Give a bounding box for every malaria parasite.
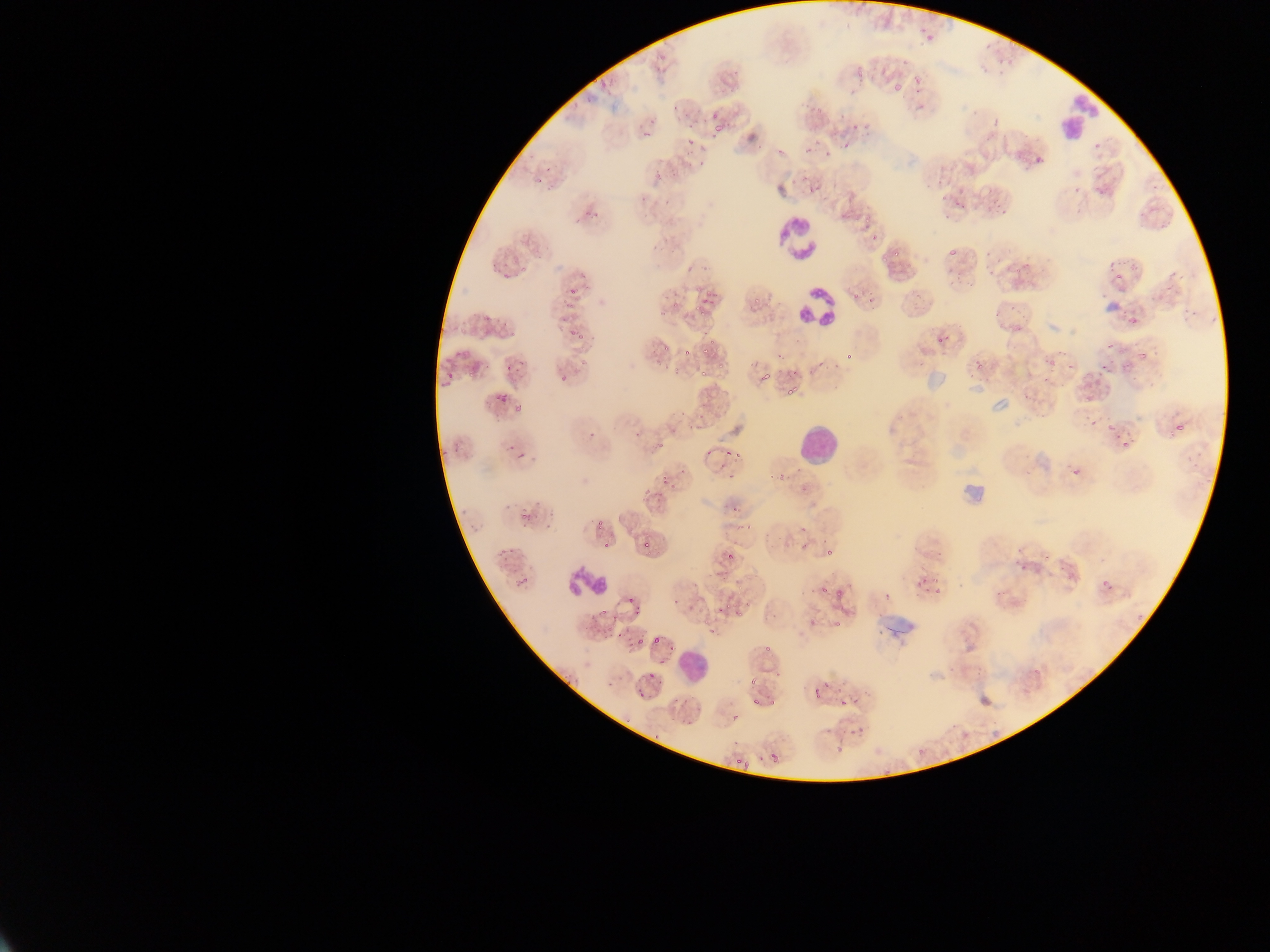
Approximate bounding boxes as (left, top, right, bottom) in pixels.
Malaria parasites (some below the resolvable threshold): (918, 27, 928, 38), (924, 32, 937, 42), (982, 38, 992, 51), (1004, 51, 1010, 71), (993, 52, 1004, 65), (652, 62, 664, 77), (856, 64, 865, 84), (893, 72, 908, 90), (596, 73, 614, 87), (912, 75, 920, 86), (804, 98, 825, 115), (710, 110, 721, 120), (838, 112, 846, 120), (685, 115, 701, 128), (713, 119, 730, 133), (641, 123, 656, 141), (865, 123, 879, 135), (853, 125, 862, 131), (842, 135, 859, 158), (684, 138, 696, 146), (801, 138, 818, 157), (696, 145, 706, 156), (775, 145, 784, 158), (822, 146, 833, 161), (1032, 149, 1045, 166), (696, 161, 705, 168), (652, 170, 660, 179), (803, 175, 817, 194), (1092, 182, 1105, 196), (663, 190, 673, 204), (952, 192, 966, 208), (1001, 197, 1014, 210), (990, 204, 1000, 217), (857, 212, 872, 230), (1159, 219, 1169, 229), (869, 233, 882, 243), (894, 248, 902, 258), (946, 248, 960, 257), (877, 254, 888, 266), (1012, 258, 1029, 275), (1104, 259, 1113, 270), (1125, 260, 1139, 269), (987, 263, 997, 275), (518, 267, 526, 275), (948, 271, 961, 288), (1170, 271, 1183, 280), (966, 281, 974, 288), (1162, 281, 1174, 294), (564, 283, 578, 295), (692, 284, 705, 295), (703, 284, 714, 305), (867, 288, 878, 307), (852, 291, 860, 303), (915, 292, 921, 301), (752, 295, 761, 307), (565, 301, 576, 314), (670, 301, 678, 309), (1008, 304, 1015, 313), (1180, 306, 1192, 321), (695, 308, 706, 318), (1126, 309, 1141, 326), (1207, 311, 1218, 323), (483, 313, 491, 320), (556, 318, 566, 322), (501, 319, 508, 330), (567, 327, 578, 338), (577, 330, 586, 344), (699, 330, 712, 338), (937, 333, 948, 344), (1104, 340, 1114, 350), (700, 342, 714, 355), (663, 345, 674, 353), (1055, 345, 1072, 357), (1151, 345, 1161, 355), (1136, 346, 1151, 363), (682, 348, 691, 358), (846, 348, 857, 363), (1115, 349, 1124, 357), (778, 355, 783, 363), (972, 357, 988, 371), (1046, 358, 1060, 369), (832, 361, 842, 372), (814, 362, 823, 368), (1066, 362, 1075, 373), (1099, 362, 1107, 375), (482, 363, 493, 371), (1119, 363, 1127, 373), (504, 365, 510, 375), (671, 369, 682, 377), (697, 370, 708, 377), (803, 371, 809, 379), (759, 373, 773, 384), (443, 374, 453, 383), (559, 374, 568, 382), (785, 388, 795, 396), (489, 390, 508, 406), (1085, 395, 1094, 403), (513, 406, 524, 412), (697, 408, 705, 422), (1088, 421, 1097, 429), (1175, 422, 1186, 433), (688, 423, 696, 433), (1105, 423, 1116, 436), (587, 431, 595, 439), (656, 440, 666, 447), (1119, 440, 1130, 451), (505, 443, 516, 456), (722, 450, 732, 458), (734, 452, 741, 466), (515, 453, 529, 459), (1070, 467, 1078, 475), (678, 468, 696, 485), (721, 472, 738, 482), (660, 474, 672, 487), (778, 475, 787, 482), (800, 486, 808, 494), (639, 490, 650, 502), (731, 495, 745, 514), (517, 505, 535, 530), (596, 519, 605, 529), (735, 524, 753, 537), (799, 524, 807, 531), (641, 540, 652, 548), (496, 541, 508, 564), (797, 541, 808, 551), (824, 547, 839, 560), (723, 548, 743, 566), (1042, 557, 1050, 565), (1012, 559, 1020, 570), (716, 572, 725, 580), (932, 573, 946, 602), (518, 574, 529, 586), (916, 575, 929, 586), (1102, 581, 1110, 591), (800, 584, 807, 595), (831, 585, 849, 599), (818, 587, 827, 598), (882, 590, 891, 600), (994, 590, 1002, 598), (672, 597, 679, 605), (625, 600, 636, 608), (718, 601, 735, 613), (630, 605, 641, 618), (734, 607, 749, 616), (835, 607, 843, 612), (804, 616, 812, 624), (835, 619, 844, 628), (603, 621, 612, 633), (707, 628, 714, 639), (651, 635, 666, 646), (636, 636, 645, 646), (622, 638, 630, 651), (669, 643, 675, 652), (657, 656, 665, 666), (772, 666, 779, 677), (646, 668, 656, 681), (743, 678, 760, 684), (607, 680, 613, 688), (820, 680, 828, 688), (814, 688, 822, 697), (635, 690, 643, 698), (860, 690, 869, 696), (751, 697, 761, 706), (769, 697, 777, 707), (674, 699, 682, 707), (838, 699, 849, 706), (730, 709, 742, 729), (683, 717, 695, 731), (846, 727, 856, 737), (825, 729, 834, 737), (769, 753, 779, 762), (732, 756, 742, 765), (752, 756, 761, 764) | approximate (x, y) pixel centers of objects too small to bound: (920, 108), (712, 138), (943, 197), (644, 200), (504, 277), (794, 371), (638, 434), (709, 452), (607, 545), (940, 554), (1025, 567), (603, 614), (767, 648), (856, 700), (860, 728), (656, 736).

{
  "preparation": "thin blood film",
  "field_of_view": "single",
  "image_size": "1270×952 pixels",
  "capture": "mobile-phone photograph through a microscope",
  "country": "Ghana",
  "leukocyte_locations": "approximate bounding boxes as (left, top, right, bottom) in pixels: (1054, 85, 1107, 147), (774, 215, 823, 261), (794, 278, 839, 331), (799, 429, 835, 462), (563, 565, 609, 599), (681, 649, 705, 677)"
}